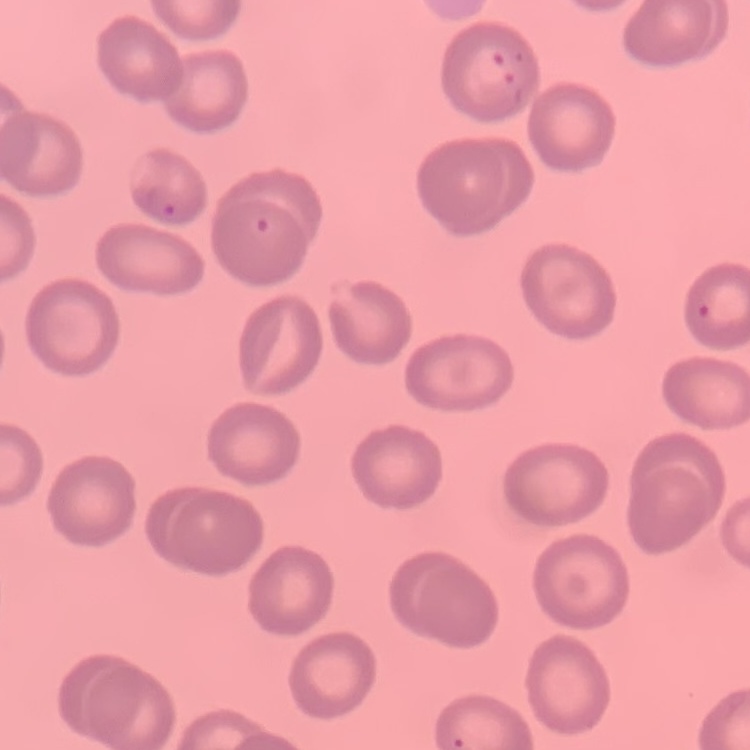
Summary:
  - Red blood cell morphology: no rouleaux formation
  - Stain: Field's or Giemsa
  - Preparation: thin blood smear
  - Image type: one tile cut from a larger photomicrograph